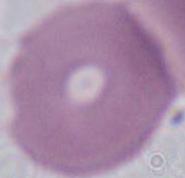

magnification = 1000x
modality = photomicrograph
identification = red blood cell